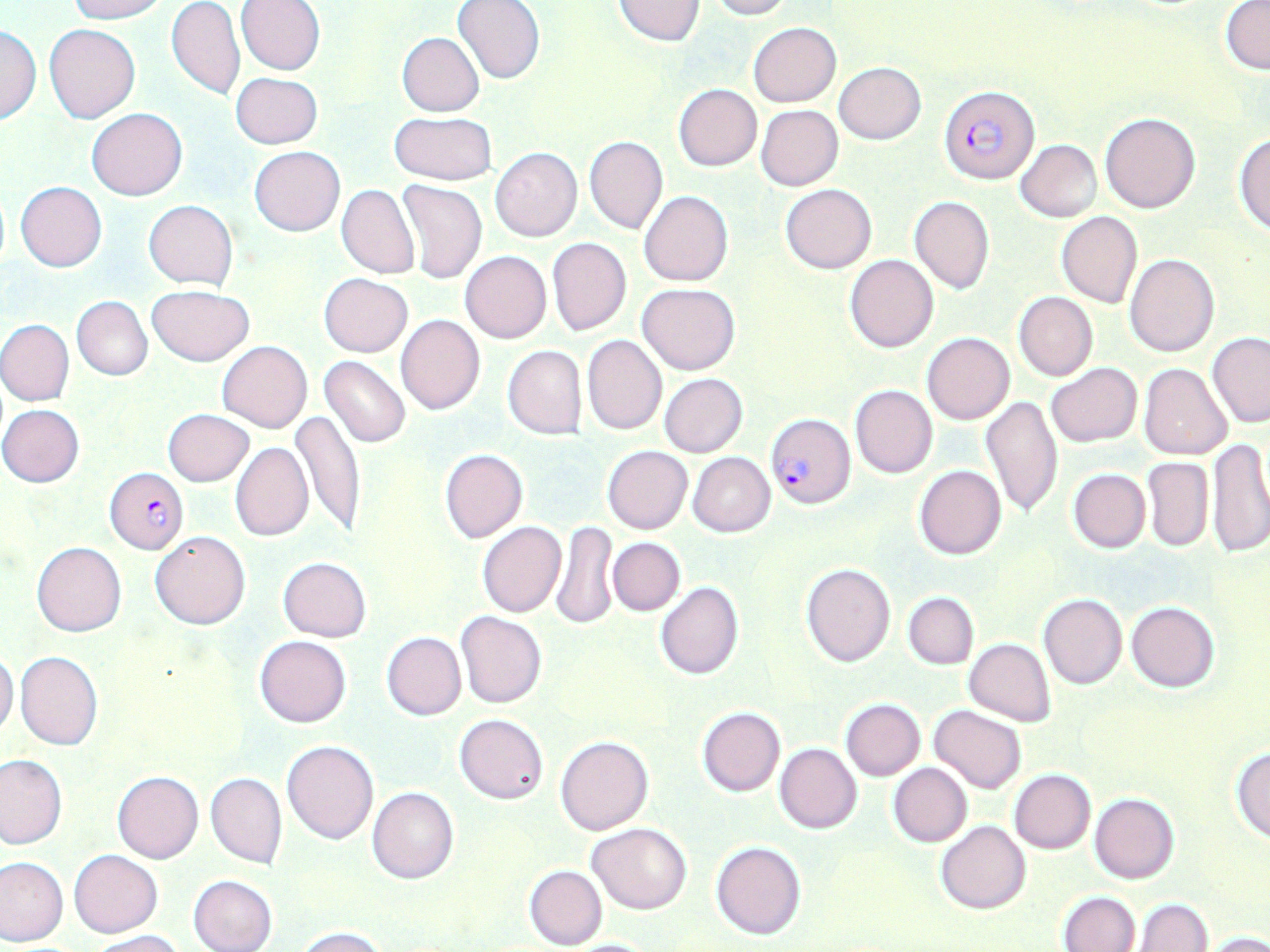

Approximate bounding boxes as [x1, y1, x2, y2] in pixels. Uninfected red blood cell locations: [66, 0, 170, 22], [236, 0, 325, 75], [613, 0, 705, 47], [708, 0, 792, 20], [1220, 0, 1269, 72], [166, 1, 244, 101], [452, 1, 545, 84], [749, 22, 841, 106], [1, 24, 40, 125], [44, 24, 140, 123], [396, 33, 484, 116], [834, 61, 925, 144], [231, 71, 321, 149], [674, 84, 762, 171], [756, 105, 843, 190], [87, 108, 186, 200], [388, 111, 497, 185], [1100, 113, 1201, 214], [1234, 132, 1270, 236], [584, 136, 668, 235], [1015, 139, 1101, 222], [250, 146, 344, 236], [490, 148, 582, 242], [396, 180, 487, 284], [15, 181, 107, 272], [781, 183, 876, 273], [337, 184, 419, 279], [640, 190, 733, 287], [910, 196, 994, 293], [143, 200, 238, 289], [1056, 211, 1143, 308], [547, 237, 631, 335], [460, 251, 552, 343], [845, 254, 938, 352], [1125, 254, 1219, 357], [319, 273, 413, 357], [638, 283, 741, 375], [147, 284, 254, 365], [1014, 293, 1097, 381], [73, 296, 152, 380], [395, 314, 485, 415], [0, 320, 74, 405], [921, 333, 1015, 425], [1207, 333, 1268, 429], [582, 335, 667, 435], [218, 340, 313, 433], [502, 345, 586, 439], [320, 356, 411, 448], [1045, 362, 1142, 447], [1138, 363, 1232, 460], [659, 373, 746, 458], [850, 385, 937, 478], [980, 396, 1063, 518], [0, 404, 85, 488], [163, 408, 254, 486], [291, 408, 365, 540], [1205, 437, 1270, 558], [231, 442, 313, 542], [602, 445, 692, 534], [439, 450, 528, 543], [688, 453, 775, 537], [1142, 457, 1214, 551], [914, 465, 1006, 559], [1067, 468, 1150, 553], [477, 522, 566, 617], [552, 522, 617, 630], [149, 530, 250, 629], [607, 537, 684, 616], [32, 541, 127, 637], [277, 557, 371, 642], [801, 563, 896, 667], [654, 581, 744, 681], [903, 592, 979, 669], [1038, 592, 1128, 690], [1126, 601, 1220, 692], [456, 610, 547, 709], [381, 632, 465, 720], [254, 635, 351, 727], [964, 638, 1056, 725], [0, 650, 19, 739], [16, 651, 103, 751], [840, 698, 925, 780], [696, 706, 785, 796], [930, 706, 1028, 794], [454, 713, 549, 803], [556, 736, 654, 836], [282, 741, 378, 843], [775, 743, 863, 834], [1230, 746, 1270, 843], [0, 754, 66, 849], [887, 763, 972, 847], [1009, 769, 1095, 853], [112, 772, 204, 863], [206, 773, 287, 869], [368, 787, 459, 884], [1088, 792, 1178, 884], [936, 821, 1030, 915], [586, 822, 692, 915], [711, 841, 807, 940], [69, 849, 162, 938], [0, 855, 68, 946], [523, 865, 607, 950], [188, 875, 277, 952], [1057, 891, 1140, 952], [1133, 898, 1212, 951], [295, 926, 387, 952], [86, 930, 185, 951], [1206, 930, 1270, 952], [563, 937, 661, 951]. Plasmodium falciparum-infected red blood cell locations: [940, 83, 1038, 185], [767, 412, 855, 509], [104, 468, 187, 555]. Slide-level diagnosis: Plasmodium falciparum. Thin blood film. Image is 1270×952 pixels. Captured at 1000x magnification. One field of a larger specimen. Light microscopy. May-Grünwald-Giemsa stain.